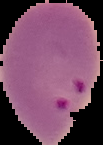
Cell region segmented out of the field of view; the surrounding area is masked to black. From a thin blood film. Image is 103×145 pixels. Malaria status: parasitized.